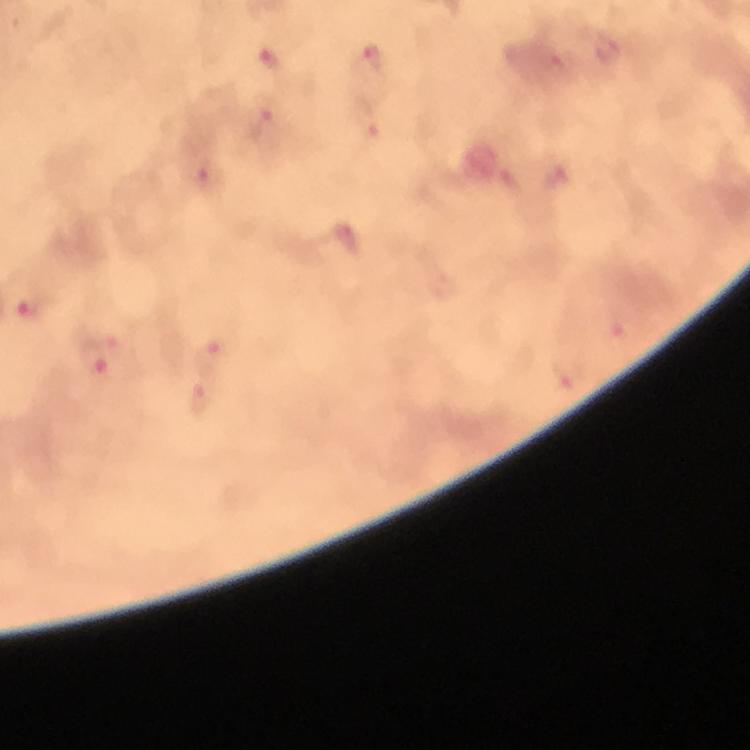

Approximate centers as {x, y} in pixels. Malaria parasite locations: {374, 58}, {271, 59}, {559, 62}, {265, 126}, {371, 126}, {556, 177}, {208, 179}, {347, 238}, {33, 312}, {618, 337}, {214, 354}, {101, 356}, {568, 374}, {203, 404}. Thick smear. 100x magnification. Photographed with a smartphone mounted on the microscope. Immersion oil was used. Image is 750×750 pixels. Giemsa stain. A crop from one field of view. From a diagnostic examination for malaria.